State which cell type is depicted.
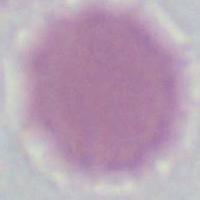
This is an erythrocyte.

modality = micrograph
magnification = 1000x